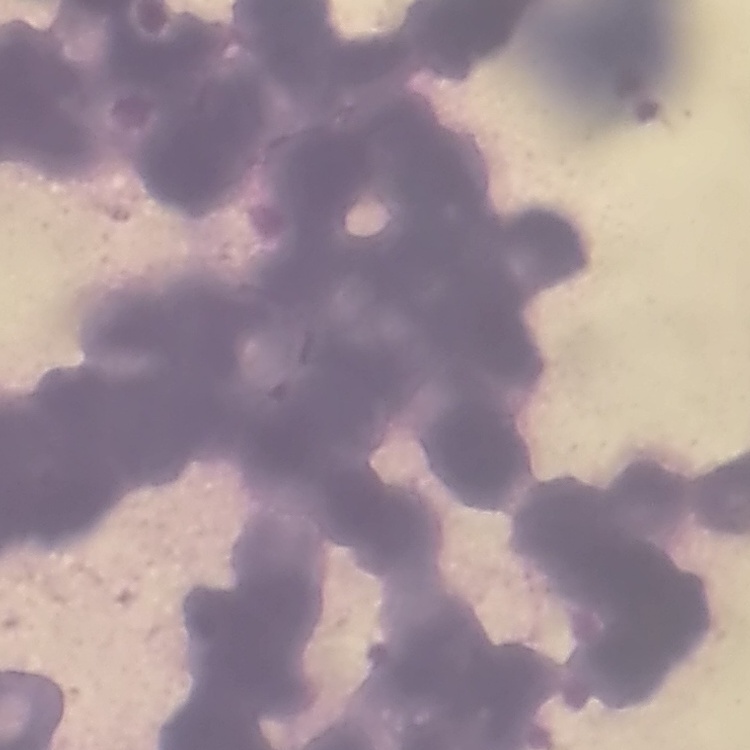
Summary:
  - Erythrocyte morphology: rouleaux formation
  - Image type: one tile cut from a larger photomicrograph
  - Preparation: thin peripheral smear
  - Stain: Field's or Giemsa